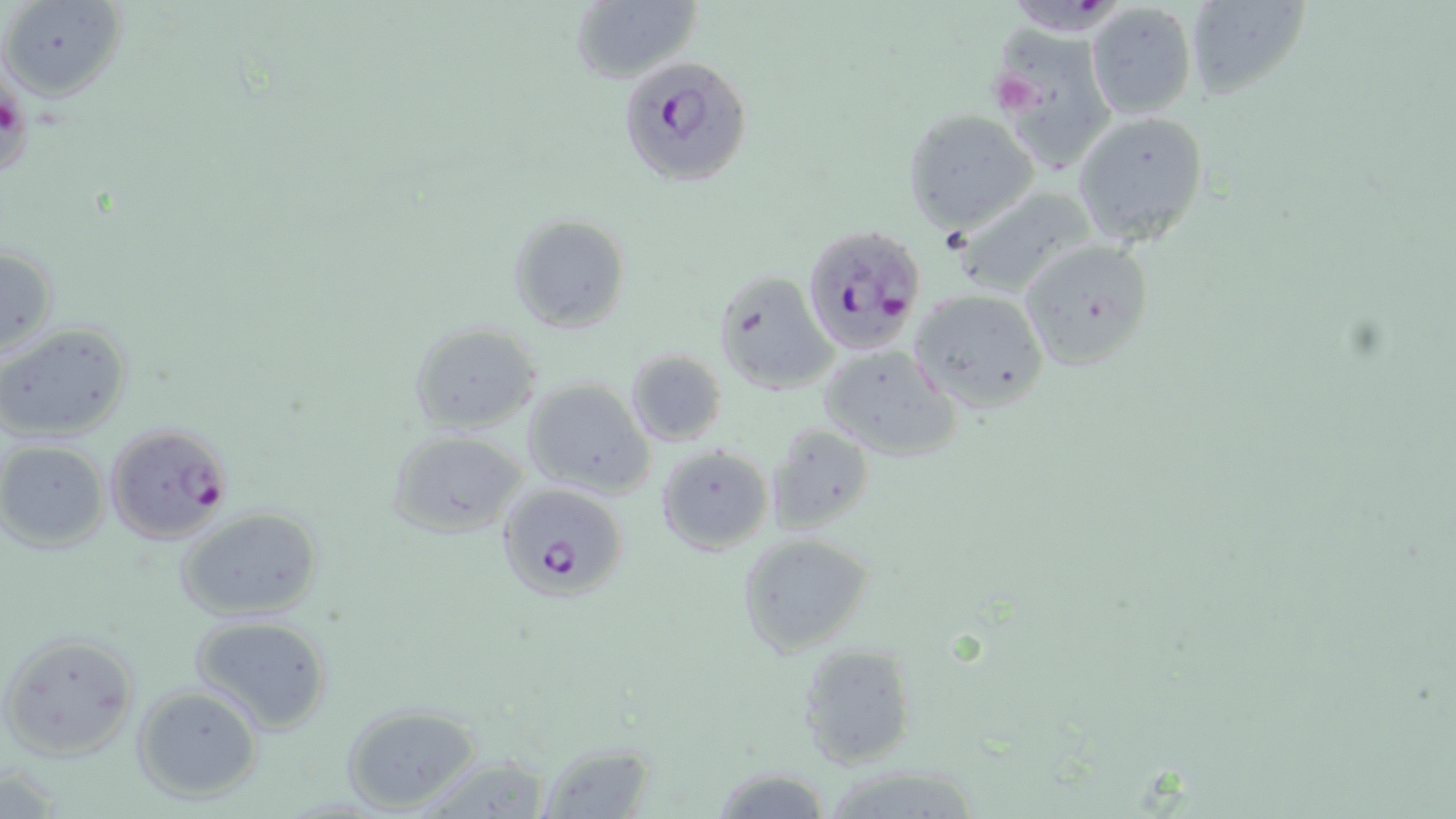

Summary:
  - Coordinate format: approximate bounding boxes as (x1, y1, x2, y2) in pixels
  - Platelet locations: (995, 75, 1042, 125)
  - Plasmodium falciparum-infected red blood cell locations: (621, 57, 753, 191), (800, 225, 929, 354), (103, 422, 234, 544), (497, 482, 628, 600)
  - Uninfected red blood cell locations: (1, 0, 125, 102), (1007, 0, 1124, 31), (1183, 0, 1312, 102), (569, 1, 699, 81), (1085, 2, 1196, 119), (985, 21, 1119, 173), (901, 109, 1038, 235), (1073, 111, 1209, 247), (954, 185, 1101, 299), (508, 213, 631, 334), (1017, 239, 1155, 371), (0, 244, 58, 360), (715, 270, 838, 395), (909, 289, 1049, 411), (0, 321, 133, 441), (408, 321, 543, 434), (816, 343, 962, 461), (624, 347, 728, 447), (521, 376, 655, 497), (769, 424, 875, 535), (385, 428, 529, 539), (0, 441, 109, 554), (656, 445, 772, 554), (175, 506, 325, 623), (739, 533, 875, 657), (189, 613, 334, 735), (0, 632, 140, 761), (796, 642, 917, 769), (133, 684, 264, 804), (342, 705, 484, 812), (534, 739, 658, 817), (412, 755, 557, 817), (706, 763, 836, 819), (818, 765, 985, 819)
  - Slide-level diagnosis: Plasmodium falciparum
  - Modality: light microscopy
  - Preparation: thin blood smear
  - Image size: 1456×819 pixels
  - Stain: May-Grünwald-Giemsa
  - Magnification: 1000x
  - Field of view: one of a larger specimen